Classify this cell by malaria status.
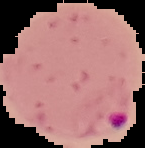

It is parasitized.

image_type: cell region segmented out of the field of view; surrounding area masked to black
image_size: 145×148 pixels
preparation: thin blood film